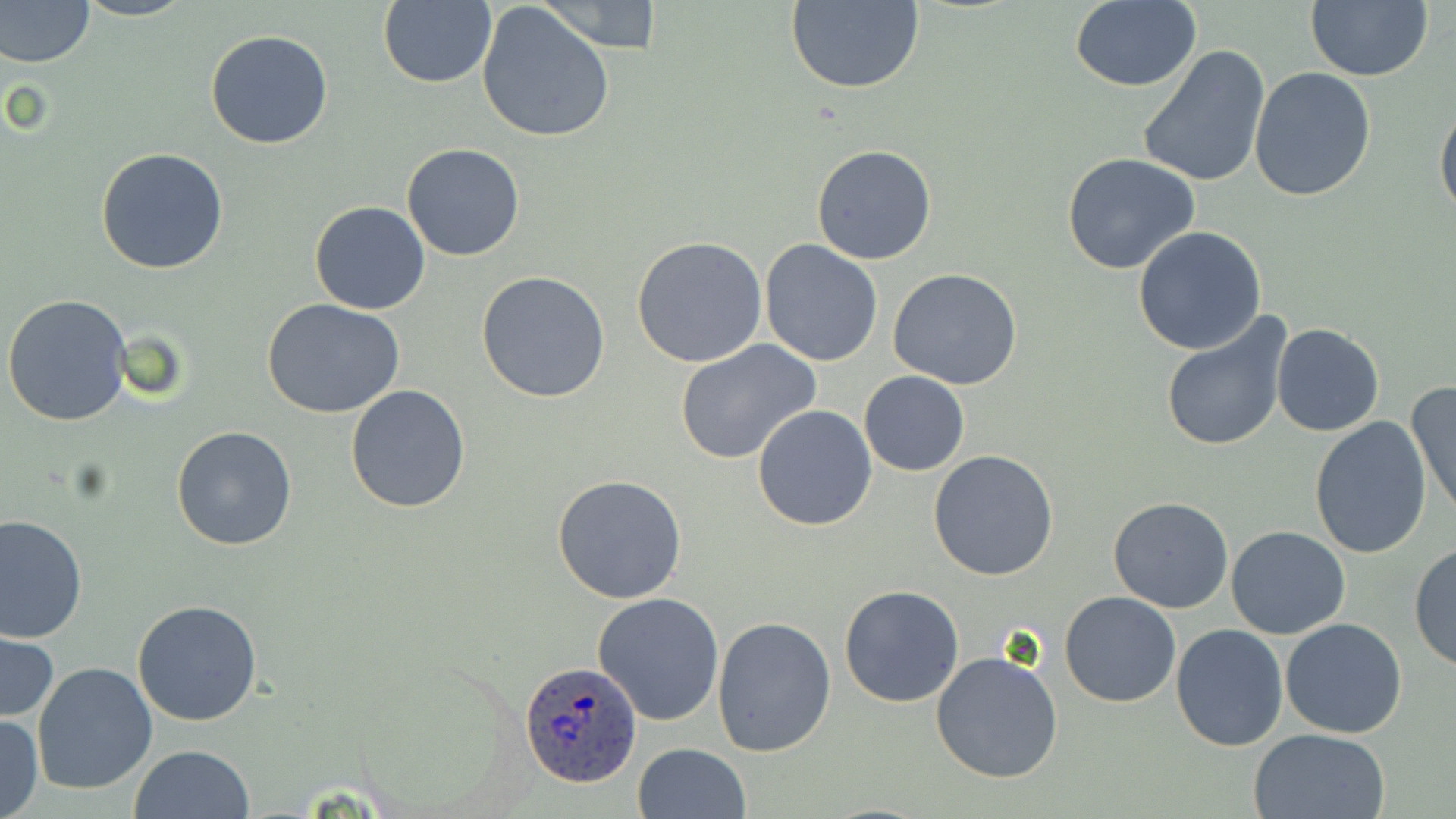

Summary:
  - Coordinate format: approximate bounding boxes as named x1/y1/x2/y2 corners in pixels
  - Uninfected red blood cell locations: (x1=0, y1=0, x2=95, y2=68), (x1=73, y1=0, x2=196, y2=22), (x1=536, y1=0, x2=662, y2=52), (x1=1068, y1=0, x2=1201, y2=91), (x1=1305, y1=0, x2=1433, y2=82), (x1=378, y1=1, x2=498, y2=88), (x1=785, y1=1, x2=925, y2=92), (x1=476, y1=2, x2=616, y2=142), (x1=204, y1=28, x2=333, y2=149), (x1=1136, y1=45, x2=1271, y2=190), (x1=1248, y1=67, x2=1377, y2=201), (x1=1435, y1=99, x2=1456, y2=224), (x1=402, y1=142, x2=525, y2=261), (x1=810, y1=143, x2=937, y2=266), (x1=95, y1=147, x2=229, y2=274), (x1=1061, y1=154, x2=1203, y2=276), (x1=308, y1=201, x2=432, y2=315), (x1=1133, y1=227, x2=1268, y2=355), (x1=630, y1=237, x2=770, y2=369), (x1=760, y1=239, x2=883, y2=367), (x1=889, y1=268, x2=1022, y2=389), (x1=476, y1=271, x2=610, y2=403), (x1=3, y1=294, x2=133, y2=426), (x1=262, y1=299, x2=407, y2=421), (x1=1159, y1=312, x2=1294, y2=455), (x1=1271, y1=322, x2=1386, y2=437), (x1=675, y1=340, x2=822, y2=465), (x1=859, y1=371, x2=969, y2=475), (x1=1407, y1=380, x2=1456, y2=519), (x1=345, y1=385, x2=471, y2=514), (x1=752, y1=406, x2=878, y2=531), (x1=1310, y1=418, x2=1433, y2=560), (x1=171, y1=424, x2=296, y2=551), (x1=928, y1=449, x2=1060, y2=580), (x1=551, y1=474, x2=687, y2=604), (x1=1109, y1=495, x2=1234, y2=612), (x1=0, y1=515, x2=87, y2=644), (x1=1227, y1=526, x2=1349, y2=640), (x1=1409, y1=541, x2=1456, y2=672), (x1=839, y1=584, x2=965, y2=707), (x1=592, y1=592, x2=726, y2=727), (x1=1060, y1=592, x2=1182, y2=708), (x1=132, y1=599, x2=264, y2=725), (x1=711, y1=617, x2=837, y2=757), (x1=1279, y1=619, x2=1407, y2=739), (x1=1171, y1=625, x2=1289, y2=750), (x1=1, y1=629, x2=59, y2=724), (x1=931, y1=649, x2=1064, y2=783), (x1=32, y1=662, x2=159, y2=796), (x1=0, y1=711, x2=44, y2=819), (x1=1248, y1=728, x2=1392, y2=819), (x1=632, y1=743, x2=751, y2=819), (x1=130, y1=744, x2=254, y2=819)
  - Plasmodium ovale-infected red blood cell locations: (x1=520, y1=659, x2=642, y2=788)
  - Slide-level diagnosis: Plasmodium ovale
  - Preparation: thin blood smear
  - Stain: May-Grünwald-Giemsa
  - Modality: optical microscopy
  - Image size: 1456×819 pixels
  - Magnification: 1000x
  - Field of view: one of a larger specimen